Give the position of every leukocyte visible.
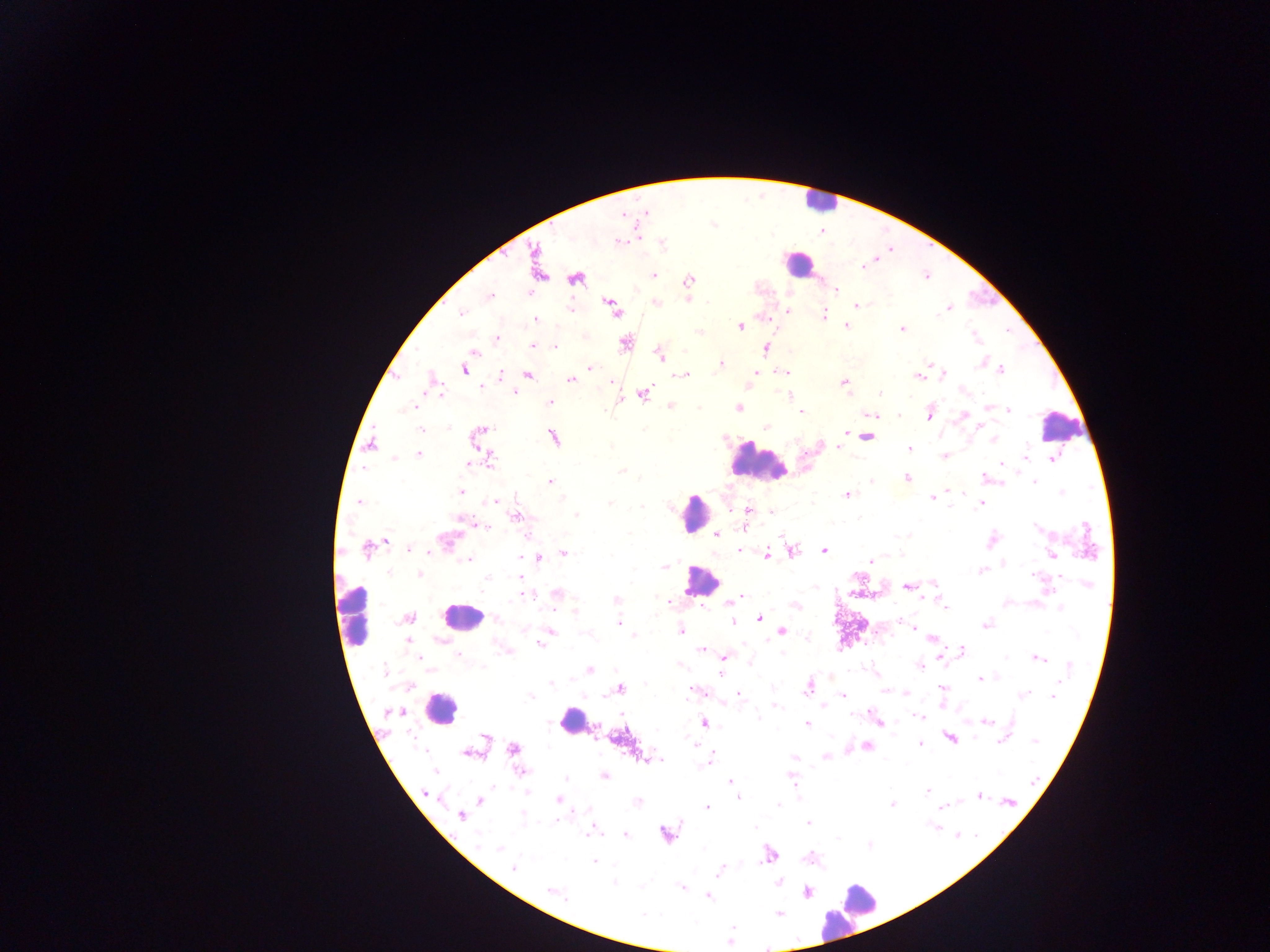

Approximate centers as {x, y} in pixels.
Leukocytes: {818, 201}, {799, 264}, {1059, 426}, {758, 462}, {694, 513}, {700, 582}, {355, 614}, {462, 616}, {440, 709}, {572, 721}, {856, 903}, {838, 923}.

Summary:
  - Plasmodium parasite locations: {619, 242}, {662, 244}, {876, 260}, {863, 266}, {653, 276}, {576, 278}, {689, 280}, {836, 290}, {528, 292}, {490, 295}, {687, 299}, {655, 303}, {611, 305}, {856, 306}, {571, 308}, {948, 308}, {787, 310}, {461, 313}, {824, 315}, {536, 320}, {740, 326}, {846, 326}, {902, 329}, {698, 332}, {975, 336}, {497, 339}, {625, 343}, {533, 347}, {554, 347}, {766, 348}, {473, 352}, {660, 355}, {929, 364}, {980, 364}, {720, 365}, {591, 368}, {465, 369}, {1001, 370}, {783, 372}, {944, 373}, {501, 374}, {527, 374}, {684, 374}, {755, 374}, {918, 375}, {571, 379}, {434, 381}, {611, 382}, {844, 383}, {480, 386}, {514, 393}, {643, 394}, {789, 395}, {880, 395}, {621, 399}, {550, 402}, {670, 406}, {988, 406}, {412, 408}, {738, 408}, {1009, 410}, {802, 411}, {930, 414}, {873, 415}, {964, 415}, {899, 416}, {765, 427}, {645, 429}, {421, 430}, {482, 430}, {845, 432}, {553, 437}, {866, 437}, {994, 439}, {371, 445}, {611, 445}, {838, 447}, {909, 448}, {418, 454}, {945, 456}, {1026, 456}, {394, 458}, {1053, 459}, {489, 460}, {469, 463}, {1003, 463}, {621, 470}, {984, 477}, {907, 478}, {871, 481}, {551, 482}, {1035, 482}, {948, 491}, {461, 492}, {1061, 493}, {848, 495}, {932, 497}, {358, 502}, {492, 502}, {611, 503}, {981, 505}, {642, 507}, {746, 510}, {772, 511}, {577, 515}, {516, 516}, {475, 524}, {481, 526}, {1036, 527}, {744, 528}, {716, 534}, {781, 535}, {386, 541}, {447, 541}, {992, 541}, {367, 549}, {408, 549}, {740, 550}, {824, 551}, {793, 552}, {564, 553}, {767, 555}, {901, 555}, {1052, 556}, {519, 558}, {540, 558}, {468, 560}, {870, 561}, {1003, 563}, {665, 566}, {980, 571}, {388, 572}, {420, 574}, {1036, 575}, {1059, 576}, {488, 578}, {520, 579}, {933, 583}, {1087, 585}, {907, 587}, {557, 594}, {526, 595}, {741, 597}, {616, 599}, {666, 599}, {728, 604}, {795, 607}, {946, 608}, {1060, 609}, {575, 611}, {408, 618}, {759, 619}, {898, 621}, {733, 622}, {619, 623}, {985, 625}, {914, 628}, {681, 631}, {782, 631}, {551, 632}, {634, 636}, {806, 637}, {768, 639}, {932, 639}, {408, 641}, {541, 643}, {700, 649}, {963, 650}, {509, 652}, {782, 653}, {458, 655}, {940, 656}, {419, 657}, {725, 657}, {1005, 657}, {1038, 658}, {750, 662}, {679, 665}, {920, 666}, {1070, 666}, {482, 667}, {590, 669}, {383, 671}, {721, 673}, {980, 680}, {552, 683}, {646, 685}, {942, 687}, {620, 689}, {808, 689}, {693, 691}, {885, 691}, {906, 693}, {739, 694}, {1023, 694}, {843, 695}, {530, 696}, {1053, 696}, {776, 706}, {823, 706}, {391, 712}, {757, 716}, {920, 716}, {877, 722}, {986, 722}, {703, 723}, {807, 723}, {950, 738}, {486, 740}, {999, 741}, {1034, 741}, {694, 743}, {920, 744}, {867, 746}, {513, 749}, {468, 752}, {826, 756}, {794, 758}, {649, 759}, {658, 760}, {710, 760}, {435, 771}, {522, 771}, {604, 776}, {792, 777}, {566, 779}, {731, 781}, {1033, 781}, {927, 791}, {527, 792}, {426, 794}, {979, 795}, {737, 798}, {480, 800}, {558, 800}, {637, 802}, {1010, 802}, {891, 804}, {779, 805}, {941, 806}, {707, 808}, {461, 816}, {808, 823}, {932, 826}, {756, 827}, {594, 829}, {625, 834}, {665, 834}, {957, 834}, {976, 834}, {838, 839}, {478, 844}, {869, 844}, {499, 847}, {768, 855}, {594, 862}, {514, 868}, {719, 871}, {778, 882}, {614, 883}, {681, 887}, {551, 890}, {808, 892}, {708, 897}, {566, 898}, {643, 913}, {779, 914}, {729, 942}, {767, 947}
  - Image size: 1270×952 pixels
  - Capture: mobile-phone photograph through a microscope
  - Country: Ghana
  - Field of view: single
  - Preparation: thick blood smear